Report the malaria status of this cell.
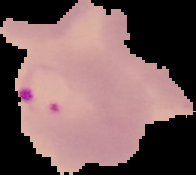

It is parasitized.

{
  "preparation": "thin blood smear",
  "image_size": "196×175 pixels",
  "image_type": "segmented cell region with the area outside set to black"
}